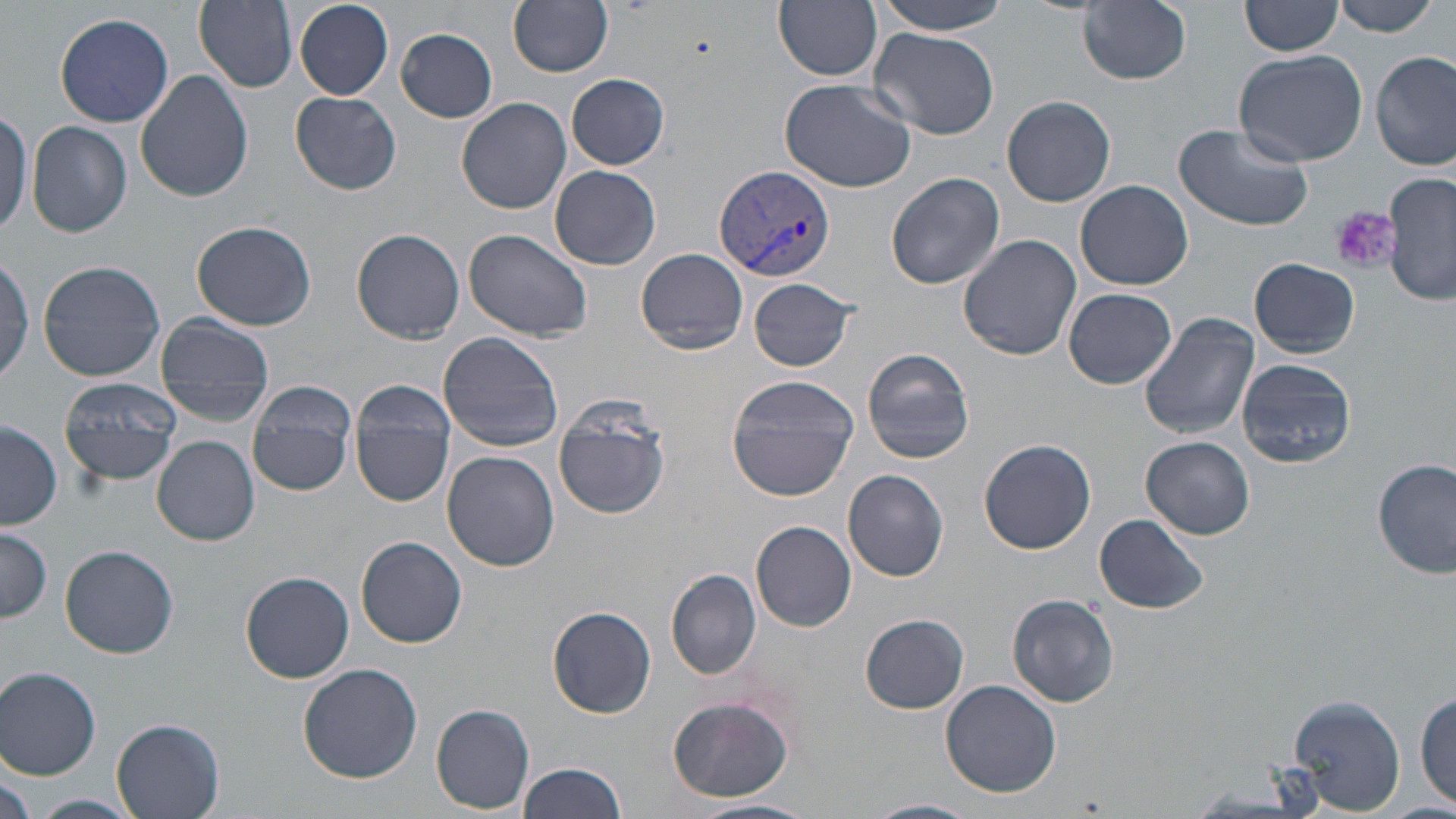

slide_level_diagnosis: Plasmodium vivax
magnification: 1000x
modality: optical microscopy
field_of_view: single
preparation: thin blood film
plasmodium_vivax_infected_red_blood_cell_locations: 'approximate bounding boxes as (x1,y1)-(x2,y2) corner pairs in pixels: (712,164)-(837,280)'
platelet_locations: 'approximate bounding boxes as (x1,y1)-(x2,y2) corner pairs in pixels: (1331,206)-(1399,275)'
image_size: 1456×819 pixels
uninfected_red_blood_cell_locations: 'approximate bounding boxes as (x1,y1)-(x2,y2) corner pairs in pixels: (194,0)-(298,90), (508,0)-(614,76), (869,0)-(1017,35), (1241,0)-(1342,56), (1332,0)-(1441,36), (295,1)-(392,100), (775,1)-(883,80), (1078,1)-(1192,86), (54,12)-(175,128), (396,27)-(498,122), (869,28)-(999,139), (1232,48)-(1372,168), (1372,51)-(1454,170), (134,71)-(252,203), (566,74)-(671,171), (779,78)-(916,194), (290,91)-(402,195), (457,96)-(571,214), (1001,96)-(1116,207), (0,109)-(32,233), (27,121)-(133,238), (1172,122)-(1315,232), (549,164)-(661,270), (886,171)-(1007,290), (1385,171)-(1455,308), (1075,180)-(1193,291), (192,220)-(317,331), (464,228)-(592,342), (352,229)-(465,343), (958,234)-(1081,362), (634,246)-(749,354), (1250,259)-(1360,356), (37,260)-(167,383), (748,277)-(859,373), (1063,287)-(1177,388), (1139,312)-(1261,440), (154,313)-(275,427), (438,332)-(565,453), (862,348)-(976,465), (1238,358)-(1356,469), (726,374)-(859,502), (59,376)-(183,487), (246,378)-(358,497), (348,380)-(457,507), (553,399)-(671,518), (1,417)-(63,529), (153,435)-(259,546), (1142,436)-(1255,539), (979,437)-(1096,554), (442,451)-(558,570), (1374,458)-(1456,580), (844,469)-(949,581), (1095,514)-(1209,614), (751,521)-(857,632), (0,527)-(52,625), (358,537)-(467,648), (60,545)-(178,657), (667,569)-(762,679), (239,572)-(354,683), (1007,594)-(1119,708), (547,607)-(657,718), (859,614)-(970,714), (297,663)-(423,784), (1,666)-(101,778), (941,678)-(1062,797), (1415,689)-(1454,811), (1284,691)-(1410,816), (667,695)-(795,803), (431,704)-(535,814), (112,717)-(227,818), (516,762)-(626,818), (0,767)-(35,819), (31,794)-(142,819), (864,798)-(980,819), (694,799)-(817,819)'
stain: May-Grünwald-Giemsa